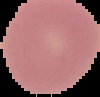 From a thin blood film. Segmented cell region on a black background. Image is 100×97 pixels. Malaria status: uninfected.